Name the cell type shown.
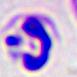

A leukocyte.

Summary:
  - Magnification: 400x
  - Modality: micrograph